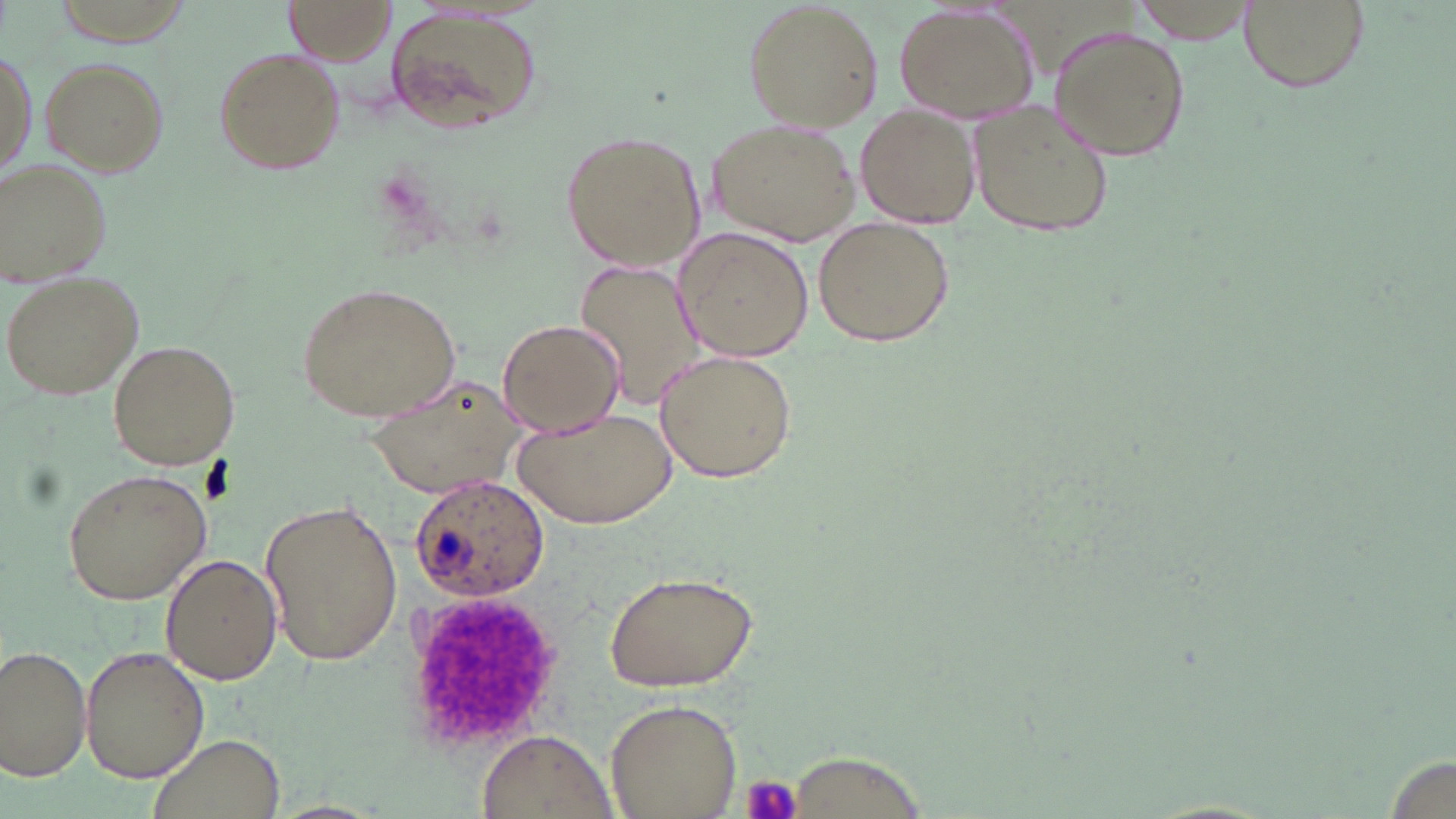

Summary:
  - Coordinate format: approximate bounding boxes as named x1/y1/x2/y2 corners in pixels
  - Platelet locations: (x1=404, y1=591, x2=557, y2=752), (x1=741, y1=773, x2=804, y2=819)
  - Plasmodium ovale-infected red blood cell locations: (x1=408, y1=474, x2=552, y2=601)
  - Uninfected red blood cell locations: (x1=741, y1=0, x2=883, y2=131), (x1=1131, y1=0, x2=1257, y2=42), (x1=1237, y1=0, x2=1369, y2=93), (x1=283, y1=2, x2=393, y2=66), (x1=893, y1=5, x2=1041, y2=122), (x1=384, y1=10, x2=543, y2=138), (x1=1049, y1=24, x2=1189, y2=162), (x1=2, y1=43, x2=36, y2=186), (x1=214, y1=47, x2=345, y2=174), (x1=40, y1=55, x2=167, y2=174), (x1=968, y1=98, x2=1116, y2=242), (x1=855, y1=105, x2=979, y2=227), (x1=711, y1=119, x2=858, y2=246), (x1=560, y1=128, x2=708, y2=274), (x1=0, y1=159, x2=112, y2=286), (x1=813, y1=216, x2=955, y2=347), (x1=676, y1=228, x2=813, y2=361), (x1=575, y1=257, x2=706, y2=406), (x1=4, y1=268, x2=147, y2=400), (x1=294, y1=281, x2=462, y2=422), (x1=497, y1=317, x2=625, y2=438), (x1=107, y1=339, x2=240, y2=469), (x1=653, y1=349, x2=800, y2=484), (x1=368, y1=370, x2=528, y2=497), (x1=515, y1=403, x2=677, y2=527), (x1=63, y1=466, x2=212, y2=606), (x1=260, y1=498, x2=404, y2=667), (x1=160, y1=554, x2=282, y2=683), (x1=605, y1=570, x2=761, y2=692), (x1=0, y1=644, x2=92, y2=782), (x1=79, y1=645, x2=208, y2=782), (x1=606, y1=698, x2=742, y2=817), (x1=146, y1=731, x2=286, y2=819), (x1=477, y1=732, x2=615, y2=819), (x1=787, y1=749, x2=929, y2=817), (x1=1379, y1=753, x2=1449, y2=819)
  - Slide-level diagnosis: Plasmodium ovale
  - Image size: 1456×819 pixels
  - Magnification: 1000x
  - Field of view: one of a larger specimen
  - Stain: May-Grünwald-Giemsa
  - Preparation: thin blood smear
  - Modality: light microscopy